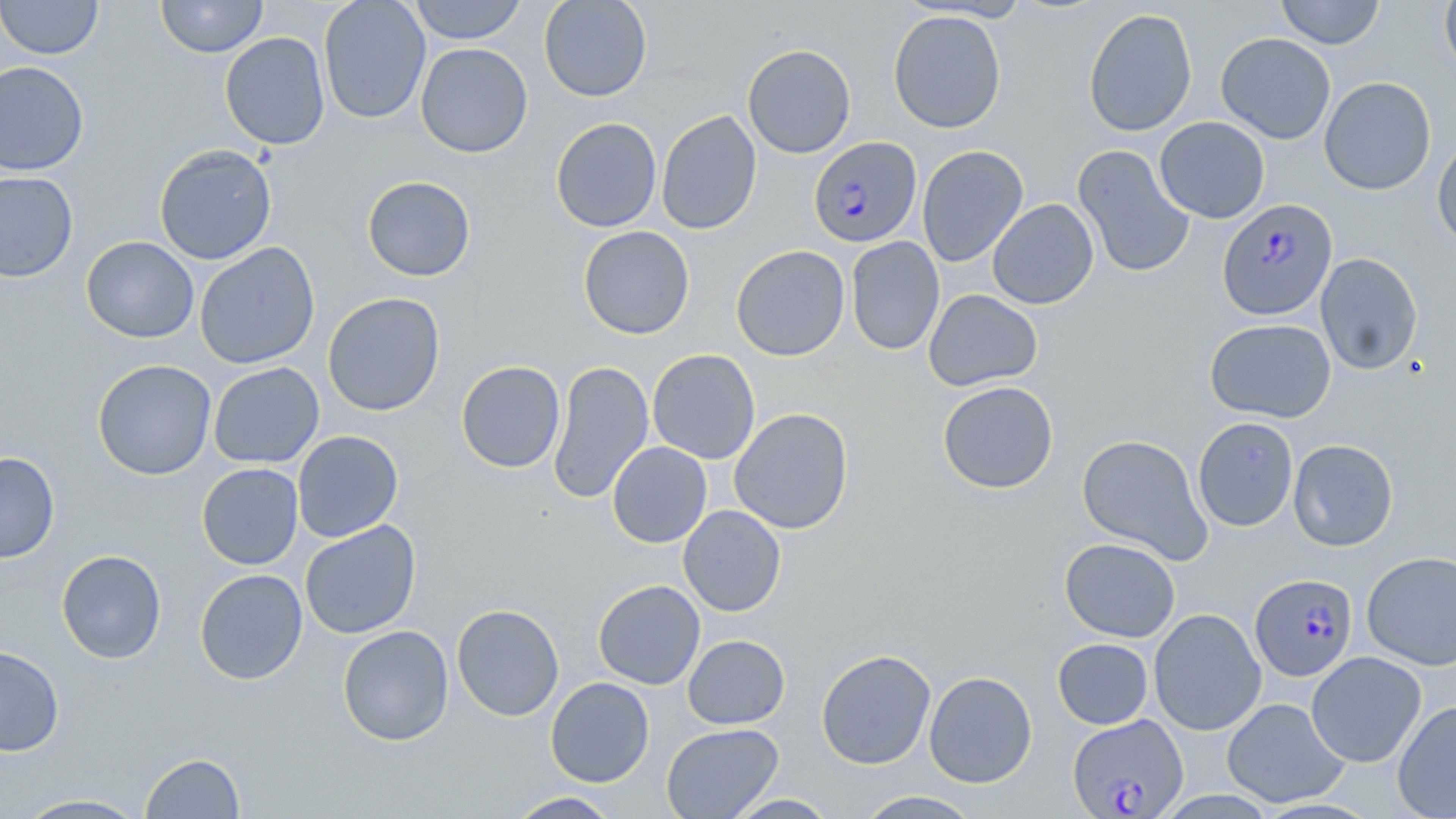
slide-level diagnosis = Plasmodium falciparum
modality = optical microscopy
uninfected red blood cell locations = approximate bounding boxes as named x1/y1/x2/y2 corners in pixels: (x1=0, y1=0, x2=103, y2=60), (x1=156, y1=0, x2=267, y2=58), (x1=318, y1=0, x2=431, y2=124), (x1=407, y1=0, x2=527, y2=44), (x1=538, y1=0, x2=653, y2=102), (x1=1276, y1=0, x2=1384, y2=49), (x1=1439, y1=0, x2=1456, y2=79), (x1=1083, y1=8, x2=1197, y2=137), (x1=888, y1=10, x2=1007, y2=133), (x1=220, y1=31, x2=331, y2=150), (x1=1215, y1=32, x2=1336, y2=144), (x1=415, y1=43, x2=533, y2=158), (x1=743, y1=44, x2=856, y2=158), (x1=0, y1=61, x2=89, y2=175), (x1=1319, y1=76, x2=1436, y2=195), (x1=656, y1=109, x2=762, y2=235), (x1=1155, y1=116, x2=1270, y2=223), (x1=550, y1=118, x2=662, y2=232), (x1=1432, y1=135, x2=1456, y2=252), (x1=154, y1=143, x2=277, y2=265), (x1=1073, y1=144, x2=1195, y2=278), (x1=917, y1=145, x2=1028, y2=266), (x1=0, y1=171, x2=78, y2=282), (x1=362, y1=176, x2=475, y2=281), (x1=987, y1=198, x2=1099, y2=309), (x1=578, y1=225, x2=695, y2=339), (x1=81, y1=236, x2=199, y2=343), (x1=846, y1=236, x2=944, y2=355), (x1=194, y1=242, x2=320, y2=369), (x1=731, y1=245, x2=850, y2=361), (x1=1315, y1=252, x2=1423, y2=375), (x1=923, y1=289, x2=1042, y2=391), (x1=322, y1=292, x2=445, y2=416), (x1=1205, y1=318, x2=1336, y2=422), (x1=648, y1=349, x2=760, y2=464), (x1=92, y1=359, x2=217, y2=480), (x1=547, y1=359, x2=654, y2=505), (x1=456, y1=360, x2=566, y2=473), (x1=208, y1=362, x2=324, y2=469), (x1=937, y1=381, x2=1058, y2=494), (x1=729, y1=408, x2=854, y2=534), (x1=1192, y1=417, x2=1299, y2=532), (x1=292, y1=430, x2=404, y2=543), (x1=1076, y1=434, x2=1213, y2=564), (x1=1288, y1=439, x2=1399, y2=551), (x1=607, y1=441, x2=712, y2=548), (x1=0, y1=452, x2=60, y2=564), (x1=197, y1=463, x2=303, y2=569), (x1=678, y1=505, x2=786, y2=617), (x1=300, y1=521, x2=421, y2=639), (x1=1059, y1=538, x2=1181, y2=642), (x1=56, y1=550, x2=167, y2=664), (x1=1361, y1=551, x2=1456, y2=671), (x1=194, y1=569, x2=308, y2=685), (x1=593, y1=579, x2=705, y2=690), (x1=451, y1=604, x2=564, y2=721), (x1=1149, y1=608, x2=1266, y2=736), (x1=337, y1=625, x2=454, y2=745), (x1=683, y1=634, x2=790, y2=729), (x1=1052, y1=638, x2=1153, y2=729), (x1=0, y1=645, x2=65, y2=757), (x1=815, y1=649, x2=937, y2=769), (x1=1306, y1=651, x2=1426, y2=768), (x1=924, y1=670, x2=1037, y2=788), (x1=545, y1=677, x2=654, y2=787), (x1=1222, y1=697, x2=1348, y2=808), (x1=1392, y1=699, x2=1456, y2=819), (x1=661, y1=723, x2=784, y2=819), (x1=140, y1=752, x2=246, y2=818), (x1=852, y1=790, x2=983, y2=819), (x1=506, y1=791, x2=624, y2=818), (x1=14, y1=794, x2=151, y2=818), (x1=724, y1=794, x2=840, y2=818)
image size = 1456×819 pixels
field of view = single
stain = May-Grünwald-Giemsa
preparation = thin blood film
magnification = 1000x
Plasmodium falciparum-infected red blood cell locations = approximate bounding boxes as named x1/y1/x2/y2 corners in pixels: (x1=809, y1=136, x2=923, y2=247), (x1=1217, y1=198, x2=1338, y2=321), (x1=1250, y1=573, x2=1358, y2=680), (x1=1067, y1=714, x2=1189, y2=818)